Identify the blood parasite species.
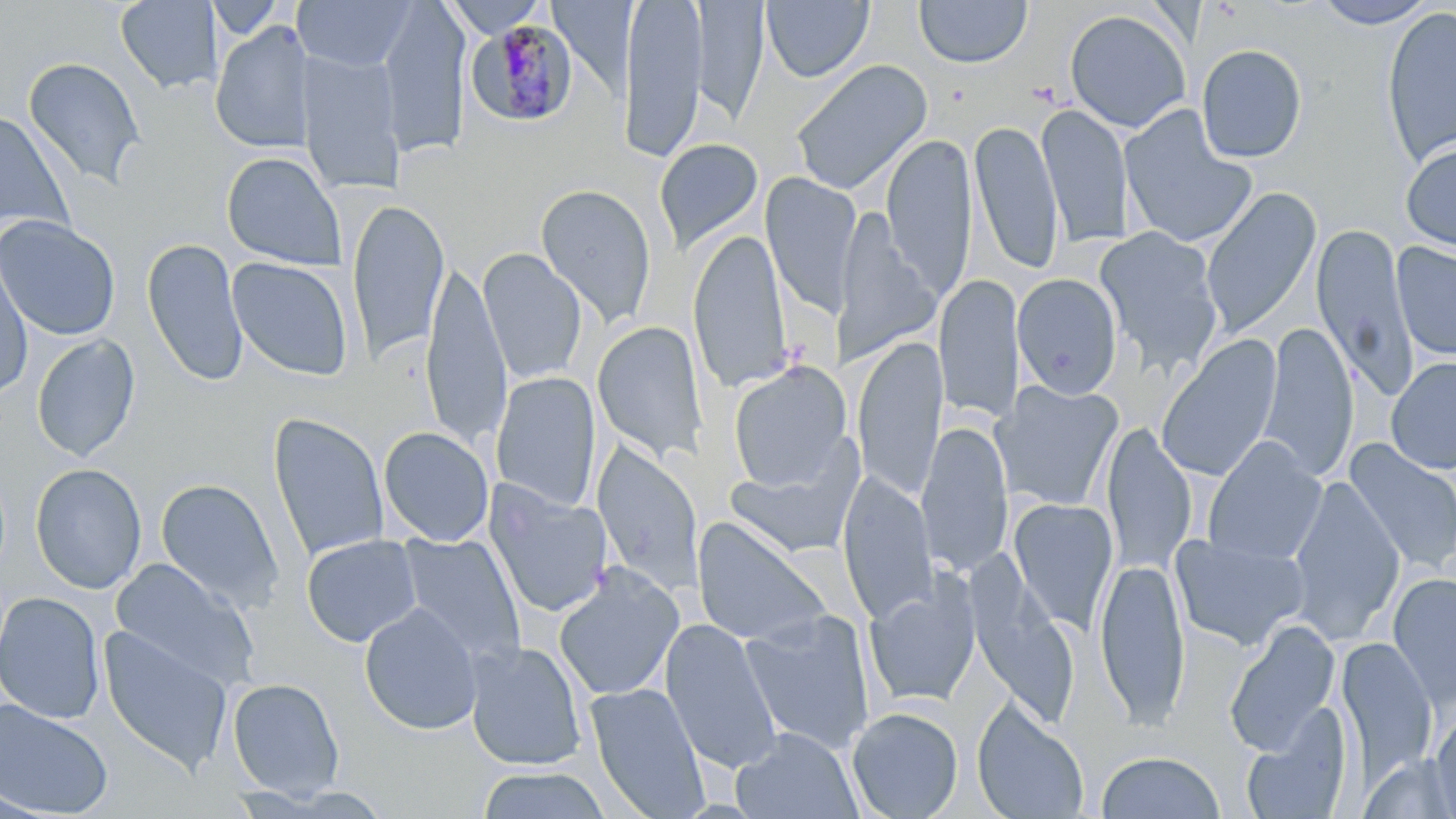
Plasmodium malariae.

Approximate bounding boxes as (x1,y1)-(x2,y2) corner pairs in pixels. Uninfected red blood cell locations: (114,0)-(222,94), (293,0)-(415,72), (378,0)-(472,158), (441,0)-(551,37), (618,0)-(708,163), (691,0)-(768,129), (549,1)-(635,99), (762,1)-(874,84), (913,1)-(1032,69), (1312,1)-(1438,29), (1380,5)-(1456,168), (1064,8)-(1191,133), (210,21)-(316,154), (1195,43)-(1308,163), (297,49)-(405,196), (22,56)-(146,189), (790,59)-(933,197), (1037,104)-(1134,248), (1119,104)-(1258,249), (0,109)-(74,240), (968,119)-(1064,275), (881,133)-(977,298), (653,138)-(764,255), (1400,139)-(1456,255), (221,151)-(347,271), (762,174)-(861,318), (535,183)-(657,329), (1200,186)-(1322,342), (347,198)-(449,363), (835,211)-(939,365), (0,215)-(121,341), (1312,223)-(1419,402), (1093,227)-(1225,377), (688,228)-(793,395), (142,237)-(248,387), (1391,242)-(1456,361), (0,248)-(35,396), (477,248)-(588,385), (227,257)-(353,381), (422,262)-(512,448), (1012,273)-(1123,399), (933,274)-(1024,423), (592,321)-(708,465), (1258,322)-(1359,483), (31,334)-(141,463), (1156,335)-(1282,482), (852,336)-(947,502), (1385,356)-(1456,474), (728,362)-(851,490), (490,372)-(602,512), (1004,380)-(1124,510), (268,412)-(389,563), (917,420)-(1013,577), (1102,423)-(1197,575), (378,426)-(494,546), (1201,437)-(1327,566), (723,439)-(864,559), (1343,439)-(1456,575), (592,442)-(704,598), (30,463)-(147,594), (837,471)-(939,623), (1286,475)-(1405,645), (155,477)-(284,612), (484,480)-(614,619), (1008,497)-(1119,634), (691,517)-(832,649), (1169,532)-(1310,652), (397,533)-(526,668), (301,534)-(422,647), (1094,556)-(1190,726), (108,558)-(259,688), (553,563)-(685,702), (969,569)-(1079,729), (1387,572)-(1456,708), (863,575)-(982,709), (0,591)-(105,724), (359,602)-(484,735), (740,609)-(876,755), (660,617)-(784,774), (1224,619)-(1341,756), (98,625)-(234,775), (1339,639)-(1439,777), (464,641)-(587,771), (226,678)-(345,801), (585,682)-(711,819), (0,698)-(114,817), (971,699)-(1090,819), (1242,705)-(1354,819), (846,707)-(964,819), (1429,709)-(1456,819), (731,728)-(862,819), (1095,751)-(1226,818), (1358,753)-(1454,818), (476,766)-(612,819). Plasmodium malariae-infected red blood cell locations: (468,19)-(579,128). Thin blood film. Single field of view. Light microscopy. Image is 1456×819 pixels. May-Grünwald-Giemsa-stained preparation. Captured at 1000x magnification.